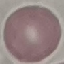
Summary:
  - Result: no malaria parasites detected
  - Image type: automatically extracted cell patch, resized to 64 × 64 pixels
  - Stain: Giemsa
  - Preparation: thin smear
  - Capture: smartphone camera at the microscope eyepiece